Classify this cell by malaria status.
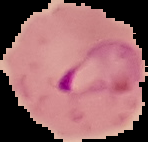
Parasitized.

Summary:
  - Image size: 148×142 pixels
  - Preparation: thin blood smear
  - Image type: cell region segmented out of the field of view; surrounding area masked to black